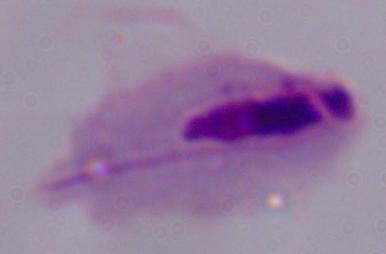

magnification = 1000x
modality = photomicrograph
identification = trichomonad